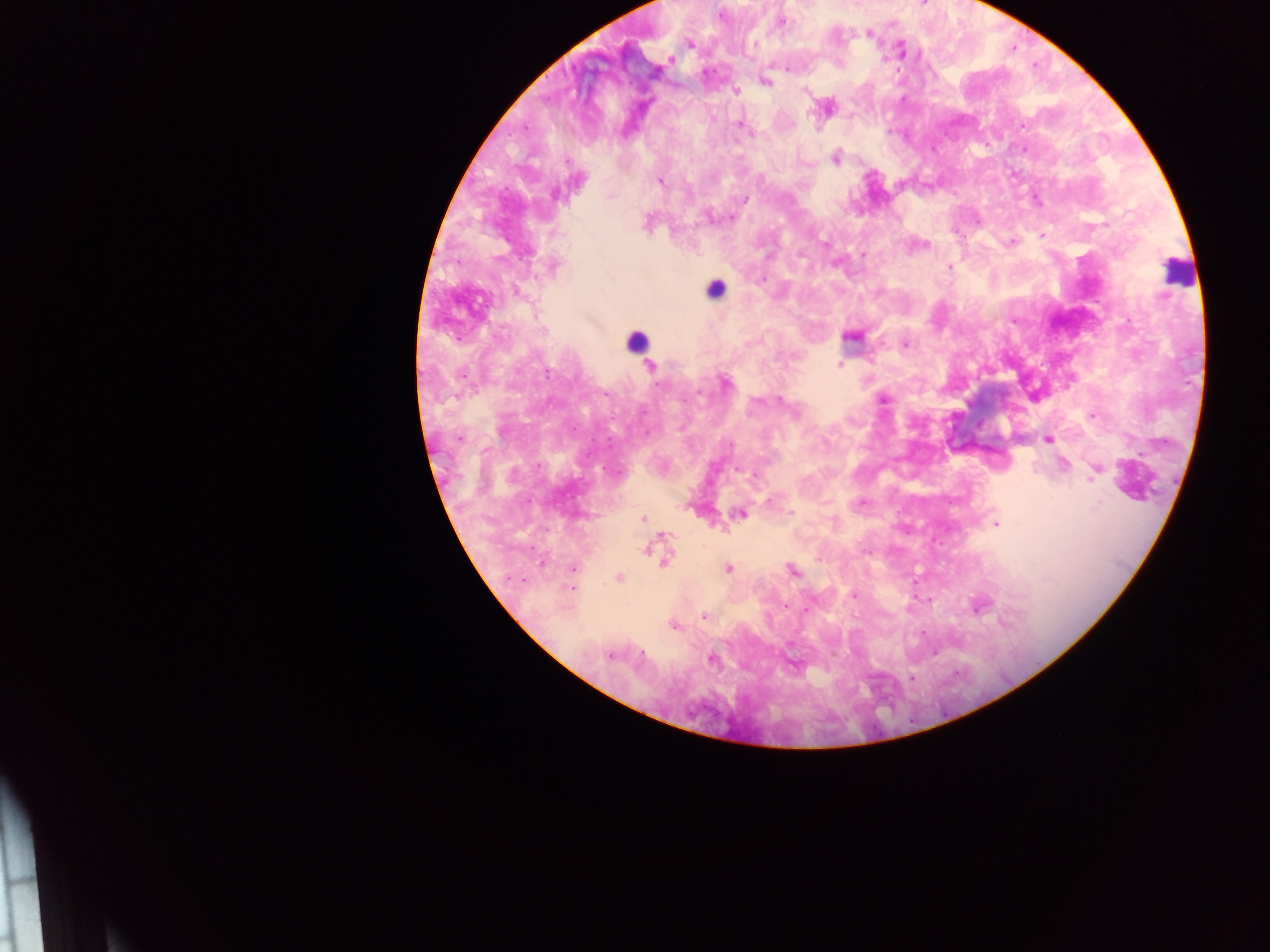
Approximate centers as {x, y} in pixels.
Summary:
  - Malaria parasite locations: {720, 16}, {782, 22}, {869, 32}, {690, 45}, {902, 49}, {670, 60}, {788, 69}, {765, 82}, {736, 91}, {740, 126}, {836, 159}, {567, 161}, {660, 181}, {556, 195}, {744, 200}, {647, 221}, {1042, 235}, {1012, 242}, {825, 244}, {800, 254}, {863, 255}, {554, 266}, {949, 267}, {763, 279}, {516, 292}, {543, 330}, {851, 336}, {904, 344}, {840, 364}, {650, 366}, {546, 374}, {725, 383}, {884, 399}, {781, 400}, {1093, 414}, {459, 438}, {1047, 440}, {730, 445}, {1063, 464}, {1097, 469}, {738, 470}, {770, 500}, {862, 501}, {740, 513}, {791, 514}, {643, 519}, {996, 524}, {663, 535}, {645, 549}, {664, 561}, {542, 563}, {573, 569}, {728, 569}, {792, 570}, {619, 578}, {572, 588}, {854, 595}, {785, 605}, {979, 607}, {806, 609}, {704, 617}, {673, 625}, {642, 654}, {610, 656}, {712, 659}, {911, 678}
  - Leukocyte locations: {1176, 270}, {715, 289}, {635, 340}
  - Country: Ghana
  - Field of view: single
  - Capture: mobile-phone photograph through a microscope
  - Image size: 1270×952 pixels
  - Preparation: thick blood smear